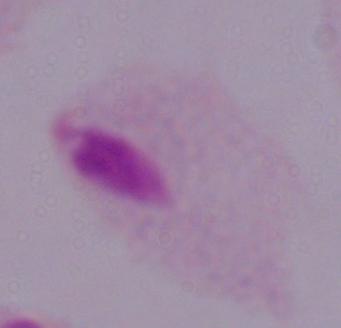

Summary:
  - Identification: trichomonad
  - Modality: micrograph
  - Magnification: 1000x